Point out each malaria parasite and each leukocyte.
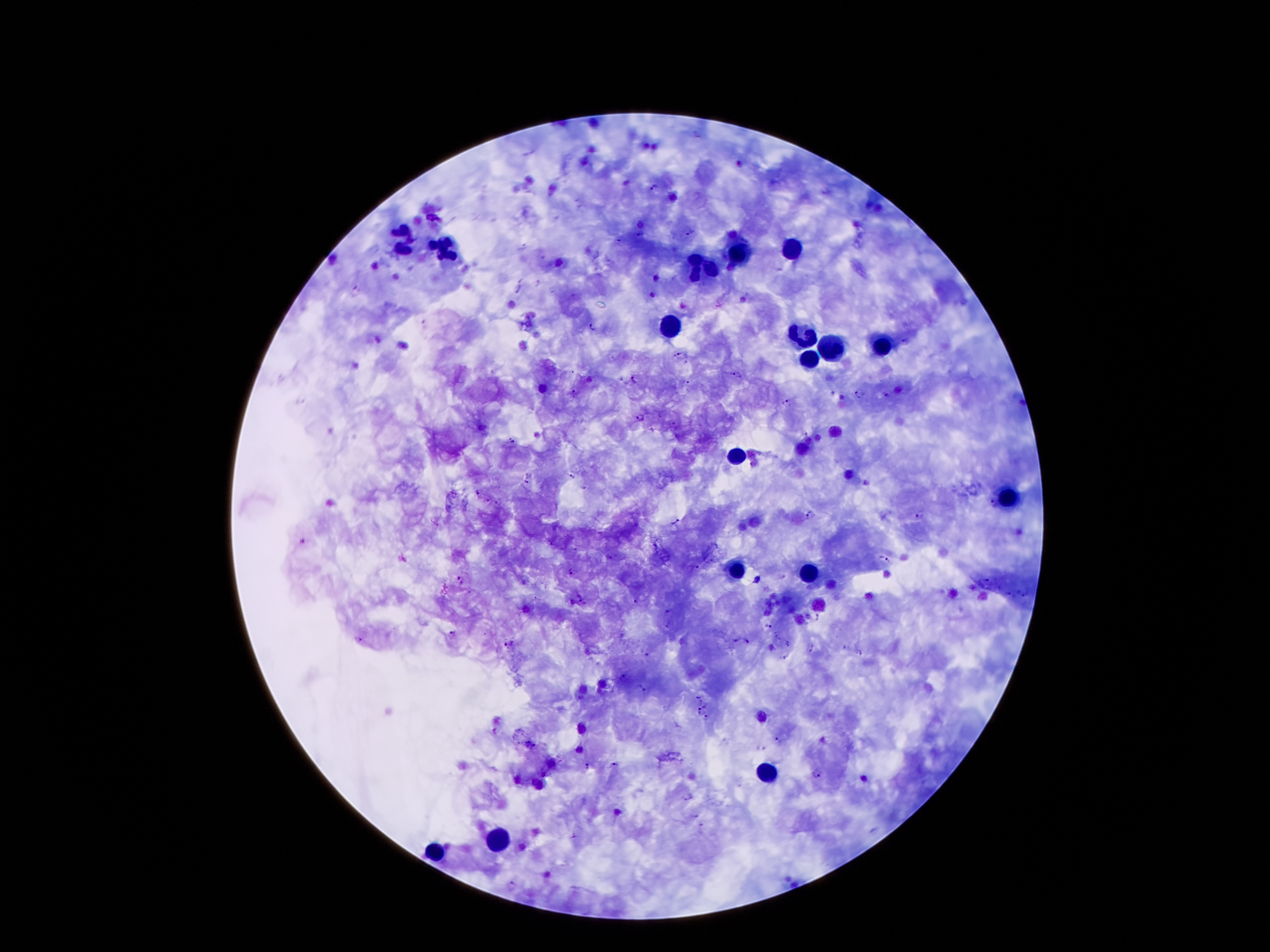

Approximate object centers, in pixels from the top-left corner.
Malaria parasites: (x=655, y=185), (x=688, y=232), (x=619, y=240), (x=538, y=283), (x=519, y=289), (x=593, y=328), (x=904, y=341), (x=681, y=355), (x=739, y=375), (x=634, y=380), (x=687, y=382), (x=572, y=390), (x=858, y=394), (x=887, y=396), (x=786, y=402), (x=640, y=418), (x=511, y=440), (x=572, y=476), (x=527, y=482), (x=585, y=487), (x=475, y=493), (x=486, y=500), (x=498, y=503), (x=992, y=505), (x=808, y=514), (x=918, y=517), (x=676, y=522), (x=303, y=541), (x=575, y=550), (x=609, y=558), (x=886, y=558), (x=695, y=567), (x=571, y=572), (x=987, y=579), (x=460, y=580), (x=758, y=580), (x=635, y=600), (x=582, y=602), (x=668, y=611), (x=819, y=616), (x=666, y=625), (x=768, y=626), (x=452, y=633), (x=620, y=636), (x=778, y=636), (x=358, y=639), (x=736, y=639), (x=747, y=641), (x=788, y=642), (x=508, y=643), (x=812, y=649), (x=859, y=652), (x=647, y=654), (x=785, y=656), (x=623, y=676), (x=644, y=689), (x=697, y=696), (x=702, y=701), (x=704, y=707), (x=698, y=710), (x=706, y=717), (x=778, y=741), (x=531, y=744), (x=762, y=748), (x=613, y=764), (x=586, y=766), (x=816, y=773), (x=690, y=797), (x=511, y=886).
Leukocytes: (x=404, y=238), (x=792, y=247), (x=447, y=250), (x=737, y=250), (x=705, y=268), (x=669, y=325), (x=801, y=336), (x=828, y=345), (x=880, y=345), (x=808, y=359), (x=735, y=456), (x=1008, y=499), (x=735, y=570), (x=808, y=572), (x=767, y=772), (x=501, y=840), (x=435, y=853).

Summary:
  - Image size: 1270×952 pixels
  - Field of view: one from this slide
  - Patient malaria status: positive for Plasmodium falciparum
  - Magnification: 100x
  - Preparation: thick blood smear
  - Capture: smartphone camera through the microscope eyepiece
  - Stain: Giemsa